Assess this cell for malaria.
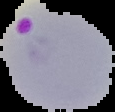

It is parasitized.

image size = 115×112 pixels
preparation = thin blood film
image type = cell region segmented out of the field of view; surrounding area masked to black